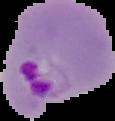

Summary:
  - Malaria status: parasitized
  - Preparation: thin blood film
  - Image size: 115×121 pixels
  - Image type: cell region segmented out of the field of view; surrounding area masked to black